Locate every Plasmodium parasite.
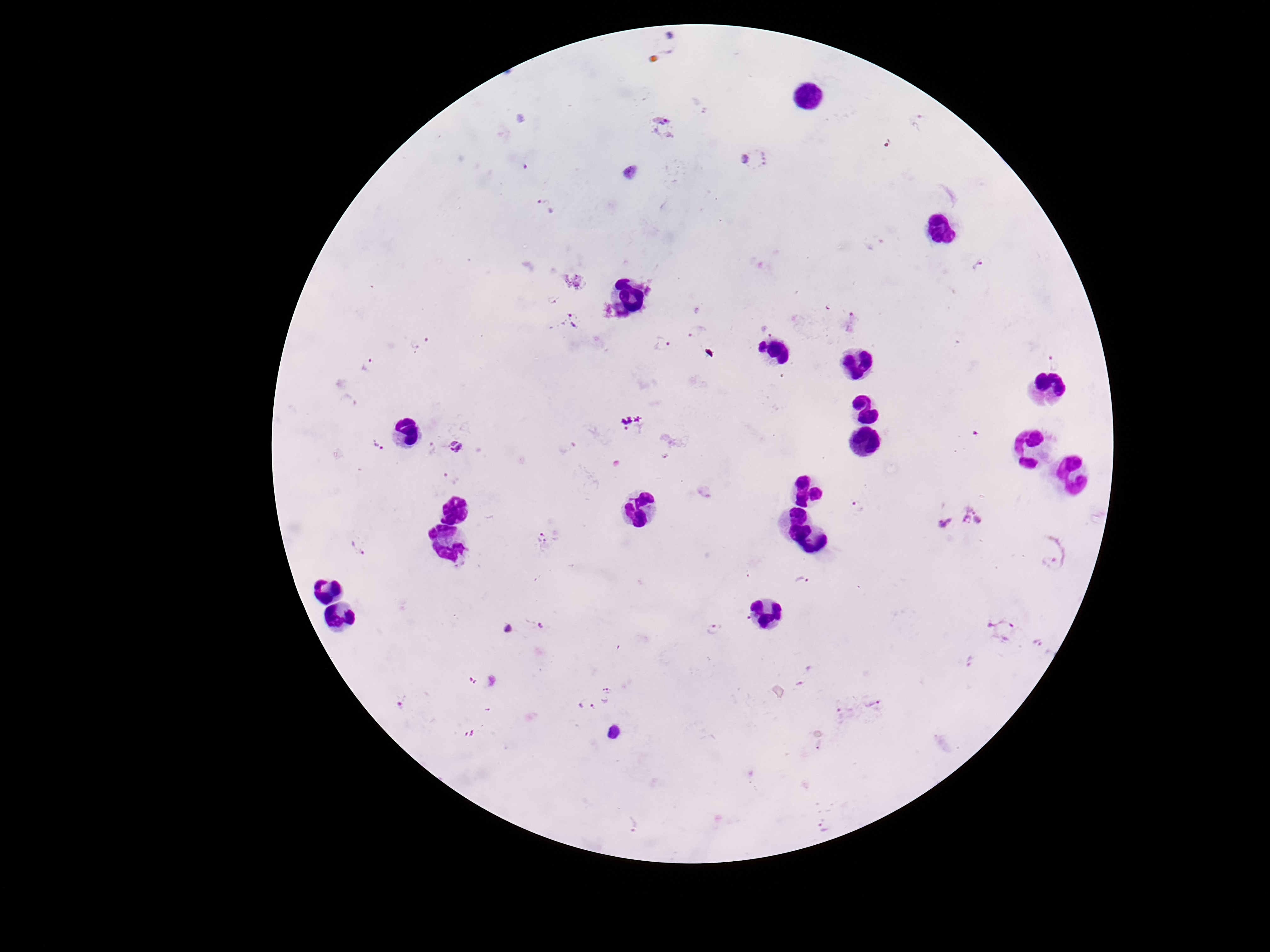
Approximate centers as {x, y} in pixels.
Plasmodium parasites: {664, 126}, {754, 159}, {544, 205}, {981, 264}, {553, 299}, {567, 322}, {769, 328}, {696, 332}, {662, 344}, {1056, 364}, {367, 365}, {630, 423}, {378, 445}, {431, 447}, {456, 447}, {666, 455}, {451, 477}, {857, 507}, {972, 515}, {941, 524}, {545, 539}, {360, 544}, {1048, 563}, {801, 577}, {522, 626}, {714, 628}, {1000, 628}, {1042, 646}, {969, 661}, {609, 694}, {401, 700}, {838, 704}, {873, 705}, {584, 706}, {613, 735}, {634, 824}, {824, 828}.

Image is 1270×952 pixels. Thick peripheral-blood smear. Giemsa-stained preparation. Patient malaria status: positive. Single field of view. Photographed through the microscope eyepiece with a smartphone camera. 100x magnification.